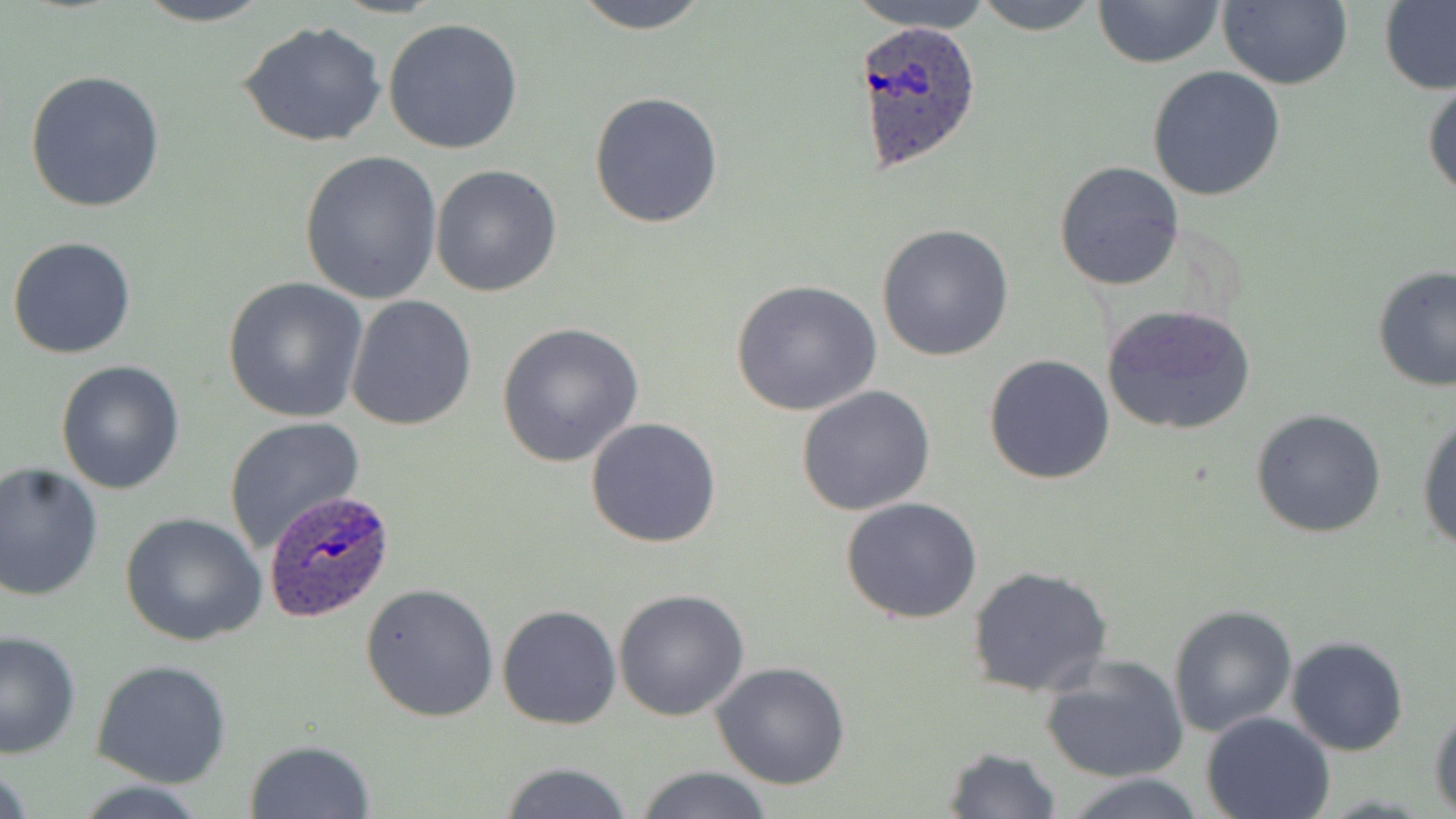
slide-level diagnosis = Plasmodium ovale
image size = 1456×819 pixels
preparation = thin blood film
uninfected red blood cell locations = approximate bounding boxes as (x1,y1)-(x2,y2) corner pairs in pixels: (123,0)-(282,26), (566,0)-(717,33), (849,0)-(997,33), (972,0)-(1104,35), (1092,0)-(1224,69), (1216,1)-(1352,89), (1379,1)-(1456,96), (382,17)-(524,155), (237,20)-(388,147), (1147,66)-(1285,200), (25,69)-(167,213), (1423,74)-(1455,203), (589,91)-(725,229), (297,152)-(444,305), (1054,160)-(1185,291), (430,165)-(562,298), (877,225)-(1016,362), (6,236)-(137,358), (1372,265)-(1456,391), (221,277)-(369,422), (730,278)-(882,416), (344,294)-(478,431), (1101,304)-(1256,436), (494,321)-(644,468), (983,354)-(1116,485), (56,359)-(185,494), (795,386)-(937,516), (1251,408)-(1387,537), (1416,410)-(1456,554), (222,416)-(367,552), (584,416)-(723,548), (0,461)-(105,602), (839,495)-(984,624), (121,512)-(265,648), (967,565)-(1114,697), (360,582)-(500,722), (612,588)-(752,722), (496,604)-(622,730), (1167,604)-(1298,738), (0,628)-(81,757), (1285,636)-(1410,756), (1041,655)-(1188,782), (93,659)-(233,789), (712,662)-(853,790), (1428,701)-(1456,815), (1200,711)-(1335,819), (244,741)-(376,819), (941,745)-(1061,819), (494,760)-(635,819), (634,765)-(774,819), (1065,773)-(1209,818)
Plasmodium ovale-infected red blood cell locations = approximate bounding boxes as (x1,y1)-(x2,y2) corner pairs in pixels: (854,18)-(984,175), (262,492)-(398,626)
stain = May-Grünwald-Giemsa
modality = optical microscopy
magnification = 1000x
field of view = one of a larger specimen